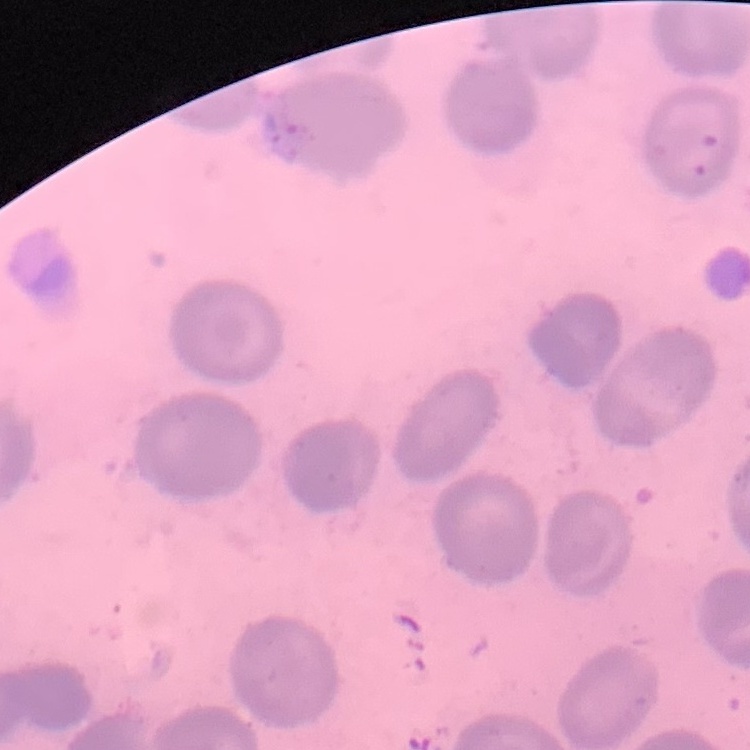

red_blood_cell_morphology: no rouleaux formation
preparation: thin peripheral smear
image_type: one tile cut from a larger photomicrograph
stain: Field's or Giemsa